State which parasite is depicted.
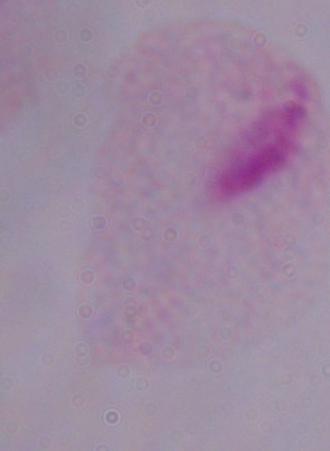

A trichomonad.

magnification = 1000x
modality = micrograph